Describe the morphology of the red blood cells.
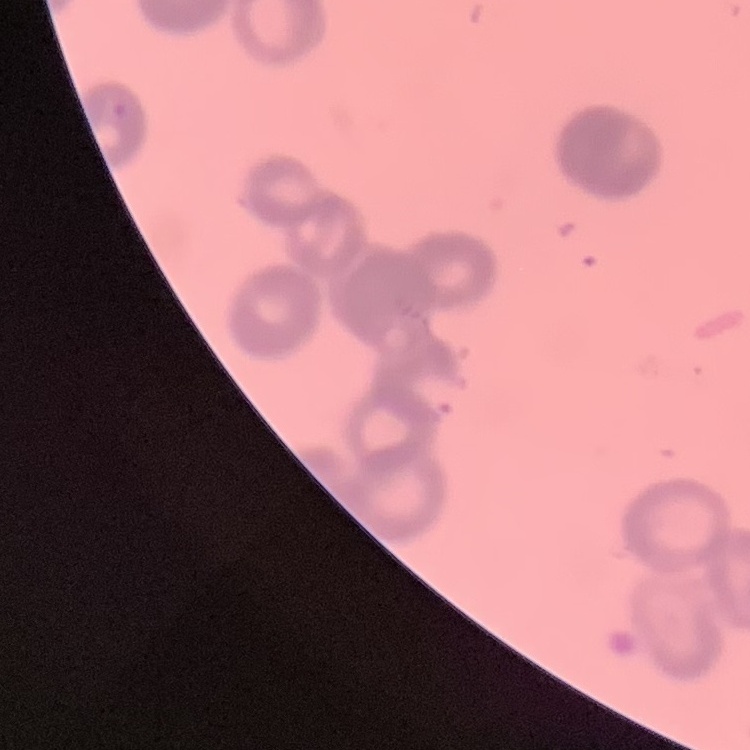

They show rouleaux formation.

One tile cut from a larger photomicrograph. Stained with either Field's or Giemsa. Thin blood film.